Name the parasite shown.
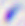

Toxoplasma gondii.

magnification = 400x
modality = micrograph